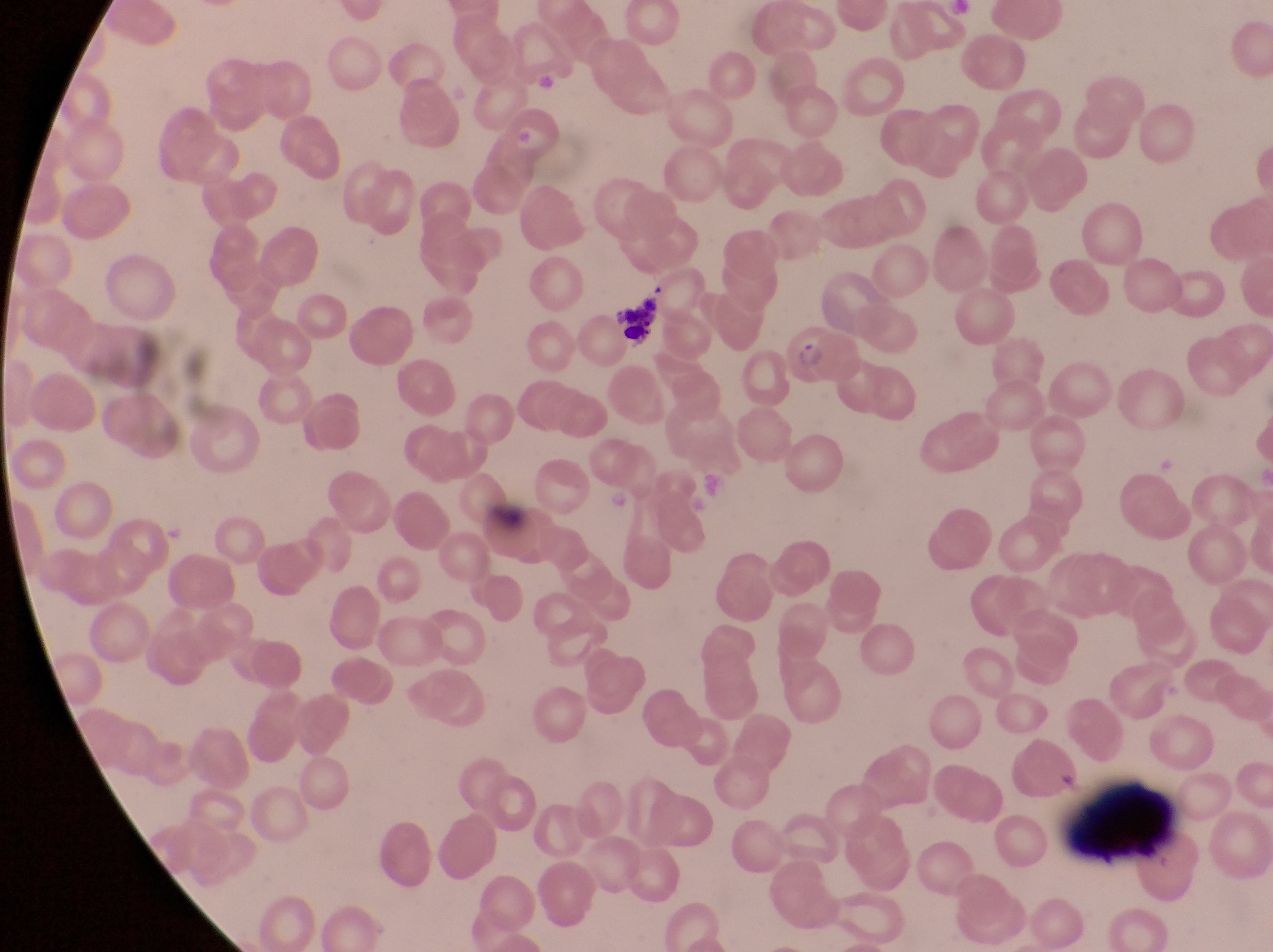

field of view = single
capture = smartphone photograph through the eyepiece of an Olympus CX-23 microscope
parasitised red blood cell locations = approximate bounding boxes as (left, top, right, bottom) in pixels: (779, 327, 859, 387)
country = Uganda
magnification = 1000x
preparation = thin blood smear
leukocyte locations = approximate bounding boxes as (left, top, right, bottom) in pixels: (612, 295, 664, 341), (1070, 778, 1186, 868)
image size = 1273×952 pixels